State which parasite is depicted.
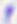
This is Toxoplasma gondii.

Summary:
  - Modality: micrograph
  - Magnification: 400x